Name the parasite shown.
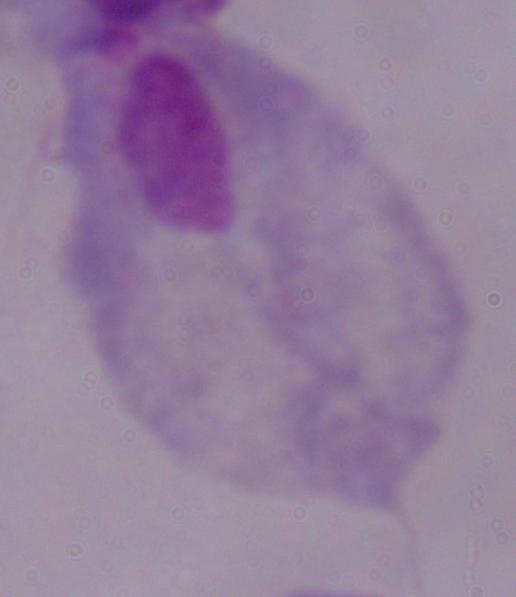
This is a trichomonad.

modality = photomicrograph
magnification = 1000x